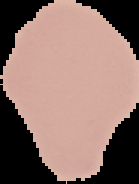
Summary:
  - Image type: segmented cell region on a black background
  - Preparation: thin blood film
  - Image size: 139×184 pixels
  - Malaria status: uninfected